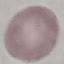
result: negative for malaria parasites
stain: Giemsa
image_type: cell patch, automatically extracted from a larger field of view and resized to 64 × 64 pixels
capture: smartphone through the microscope eyepiece
preparation: thin blood smear